Describe the morphology of the erythrocytes.
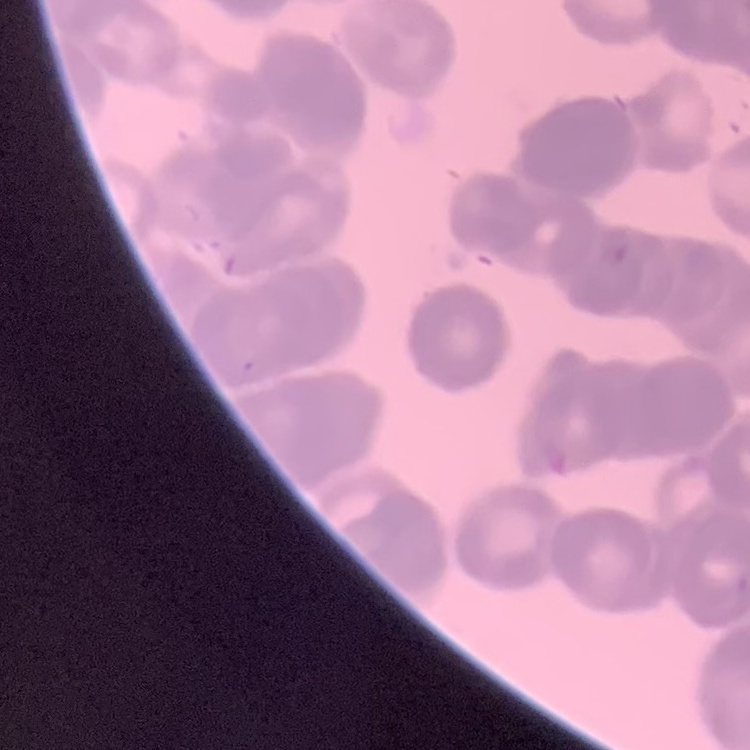
Rouleaux formation.

Summary:
  - Preparation: thin peripheral smear
  - Stain: Field's or Giemsa
  - Image type: one tile cut from a larger photomicrograph